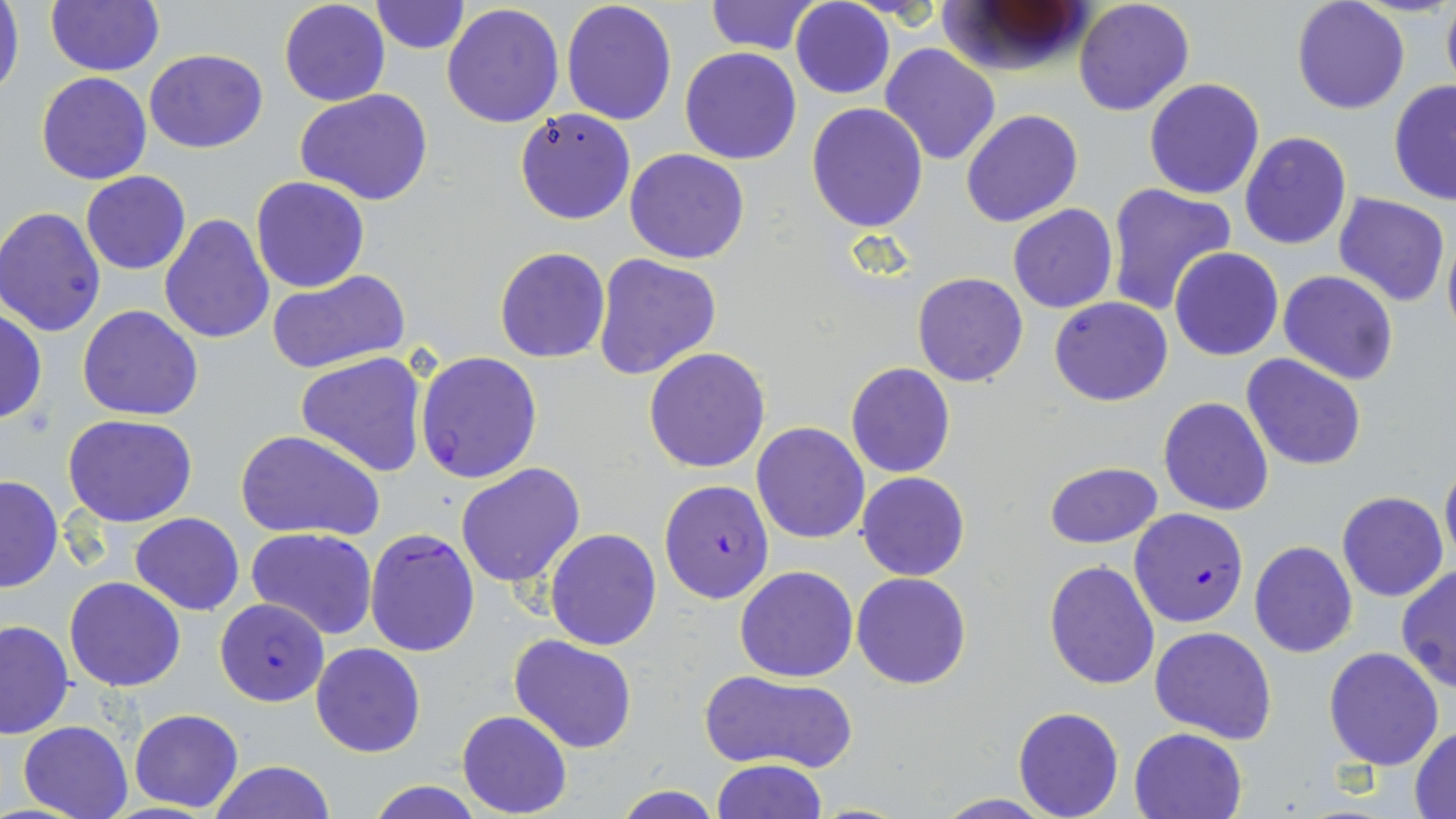
Approximate bounding boxes as named x1/y1/x2/y2 corners in pixels. Plasmodium falciparum-infected red blood cell locations: (x1=414, y1=351, x2=544, y2=484), (x1=658, y1=479, x2=774, y2=604), (x1=1129, y1=508, x2=1248, y2=628), (x1=364, y1=526, x2=481, y2=658), (x1=216, y1=598, x2=330, y2=706). Uninfected red blood cell locations: (x1=0, y1=0, x2=24, y2=105), (x1=45, y1=0, x2=164, y2=76), (x1=278, y1=0, x2=390, y2=107), (x1=1074, y1=0, x2=1195, y2=118), (x1=1441, y1=0, x2=1456, y2=95), (x1=370, y1=1, x2=470, y2=54), (x1=560, y1=1, x2=678, y2=126), (x1=704, y1=1, x2=820, y2=54), (x1=790, y1=1, x2=894, y2=99), (x1=937, y1=1, x2=1093, y2=78), (x1=1291, y1=1, x2=1410, y2=114), (x1=441, y1=4, x2=565, y2=128), (x1=880, y1=43, x2=1003, y2=167), (x1=679, y1=46, x2=804, y2=165), (x1=144, y1=48, x2=268, y2=154), (x1=36, y1=72, x2=153, y2=185), (x1=1143, y1=77, x2=1266, y2=199), (x1=1388, y1=78, x2=1456, y2=206), (x1=295, y1=90, x2=435, y2=205), (x1=806, y1=102, x2=929, y2=231), (x1=514, y1=107, x2=635, y2=224), (x1=960, y1=109, x2=1083, y2=228), (x1=1240, y1=131, x2=1352, y2=250), (x1=624, y1=148, x2=750, y2=264), (x1=80, y1=171, x2=191, y2=275), (x1=250, y1=176, x2=371, y2=293), (x1=1104, y1=182, x2=1237, y2=316), (x1=1334, y1=193, x2=1451, y2=308), (x1=1008, y1=204, x2=1118, y2=313), (x1=0, y1=207, x2=107, y2=337), (x1=158, y1=213, x2=275, y2=344), (x1=1443, y1=226, x2=1456, y2=344), (x1=495, y1=247, x2=610, y2=364), (x1=1171, y1=247, x2=1284, y2=362), (x1=592, y1=254, x2=722, y2=380), (x1=265, y1=269, x2=411, y2=375), (x1=1279, y1=269, x2=1398, y2=385), (x1=912, y1=272, x2=1029, y2=387), (x1=1049, y1=296, x2=1173, y2=406), (x1=78, y1=304, x2=202, y2=422), (x1=0, y1=307, x2=45, y2=424), (x1=643, y1=347, x2=771, y2=473), (x1=295, y1=351, x2=428, y2=477), (x1=1242, y1=354, x2=1367, y2=473), (x1=846, y1=362, x2=956, y2=478), (x1=1158, y1=397, x2=1273, y2=516), (x1=63, y1=414, x2=199, y2=527), (x1=751, y1=423, x2=870, y2=545), (x1=234, y1=429, x2=385, y2=542), (x1=1440, y1=458, x2=1456, y2=567), (x1=1043, y1=461, x2=1162, y2=549), (x1=455, y1=462, x2=586, y2=588), (x1=857, y1=471, x2=969, y2=581), (x1=0, y1=475, x2=63, y2=594), (x1=1338, y1=491, x2=1448, y2=602), (x1=130, y1=513, x2=245, y2=615), (x1=246, y1=528, x2=378, y2=640), (x1=544, y1=528, x2=662, y2=650), (x1=1249, y1=540, x2=1357, y2=658), (x1=1044, y1=559, x2=1160, y2=688), (x1=1396, y1=563, x2=1456, y2=695), (x1=734, y1=565, x2=858, y2=681), (x1=851, y1=572, x2=972, y2=689), (x1=64, y1=576, x2=186, y2=692), (x1=0, y1=619, x2=74, y2=739), (x1=1150, y1=626, x2=1277, y2=745), (x1=510, y1=634, x2=639, y2=753), (x1=309, y1=642, x2=426, y2=759), (x1=1323, y1=646, x2=1444, y2=769), (x1=701, y1=670, x2=856, y2=773), (x1=1013, y1=707, x2=1124, y2=819), (x1=130, y1=709, x2=242, y2=812), (x1=457, y1=711, x2=572, y2=818), (x1=17, y1=719, x2=134, y2=819), (x1=1410, y1=725, x2=1456, y2=816), (x1=1129, y1=727, x2=1245, y2=819), (x1=712, y1=758, x2=826, y2=818), (x1=209, y1=760, x2=333, y2=818), (x1=365, y1=780, x2=485, y2=818), (x1=614, y1=784, x2=721, y2=818), (x1=934, y1=794, x2=1054, y2=817). Slide-level diagnosis: Plasmodium falciparum. Light microscopy. Thin blood smear. Captured at 1000x magnification. May-Grünwald-Giemsa-stained preparation. Image is 1456×819 pixels. One field of a larger specimen.